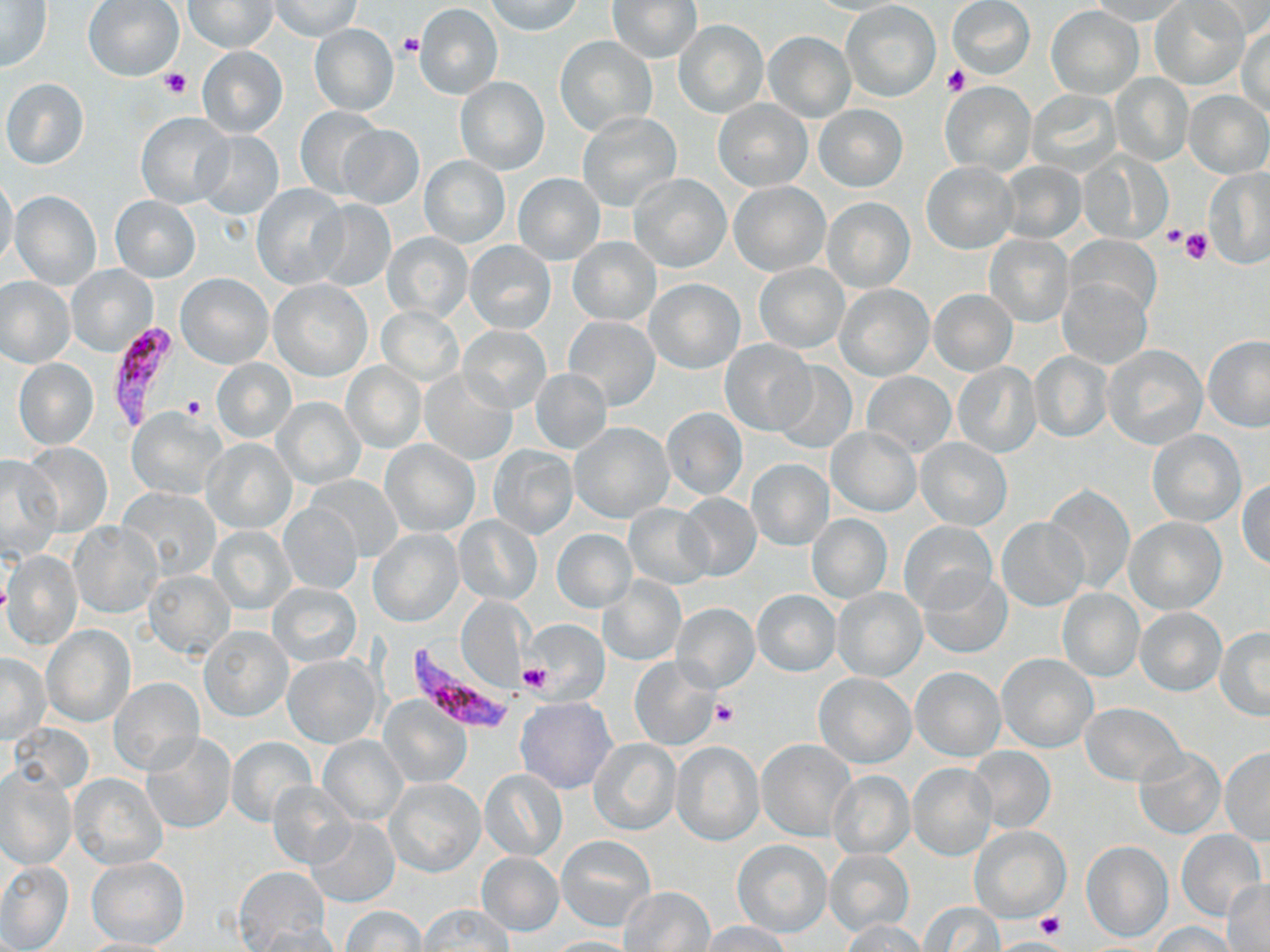

Summary:
  - Coordinate format: approximate bounding boxes as (x1,y1)-(x2,y2) corner pairs in pixels
  - Plasmodium falciparum-infected red blood cell locations: (104,322)-(182,434), (407,650)-(520,737)
  - Uninfected red blood cell locations: (83,0)-(184,82), (186,0)-(276,53), (268,0)-(362,41), (607,0)-(703,63), (948,0)-(1035,79), (1087,0)-(1190,24), (1149,0)-(1251,91), (1195,0)-(1270,40), (1,1)-(53,72), (485,1)-(584,37), (842,1)-(941,102), (415,3)-(504,98), (1046,4)-(1144,98), (674,20)-(767,118), (1238,22)-(1270,118), (309,23)-(398,116), (764,31)-(855,121), (555,35)-(657,135), (197,47)-(287,138), (1111,73)-(1192,164), (454,77)-(550,175), (1,78)-(89,169), (940,81)-(1036,175), (1026,89)-(1121,176), (1184,89)-(1269,178), (714,99)-(812,191), (814,104)-(907,191), (293,105)-(384,200), (576,112)-(681,212), (136,113)-(234,209), (337,125)-(425,209), (196,131)-(284,220), (1081,152)-(1171,245), (420,155)-(510,248), (921,162)-(1017,253), (997,162)-(1086,243), (1204,169)-(1270,268), (513,173)-(604,265), (630,173)-(731,272), (0,176)-(19,271), (729,181)-(831,277), (252,184)-(348,290), (10,191)-(102,291), (110,196)-(200,282), (823,196)-(914,291), (310,199)-(395,291), (383,231)-(474,324), (984,235)-(1073,326), (1065,235)-(1161,318), (568,238)-(660,326), (465,241)-(556,335), (755,262)-(848,353), (68,264)-(159,357), (177,273)-(273,368), (1,277)-(75,367), (8,278)-(84,451), (645,278)-(745,373), (1059,278)-(1152,368), (269,279)-(373,381), (834,284)-(934,380), (928,289)-(1018,376), (375,307)-(464,387), (562,316)-(661,412), (458,325)-(551,413), (1201,334)-(1270,433), (720,339)-(817,435), (1103,344)-(1207,449), (1029,352)-(1113,443), (13,358)-(98,449), (211,358)-(296,443), (341,361)-(425,452), (770,361)-(857,455), (952,363)-(1040,457), (420,369)-(516,465), (529,369)-(611,453), (863,372)-(955,457), (273,397)-(366,488), (660,406)-(748,501), (128,408)-(228,500), (569,422)-(674,523), (827,427)-(921,517), (1148,430)-(1246,527), (915,436)-(1012,531), (201,438)-(296,533), (381,439)-(479,537), (22,441)-(111,538), (488,446)-(578,539), (0,456)-(62,558), (746,459)-(833,550), (302,474)-(405,562), (1238,477)-(1270,570), (1044,483)-(1135,594), (120,488)-(221,578), (675,492)-(762,581), (277,502)-(362,595), (625,503)-(715,590), (807,514)-(892,603), (454,516)-(541,604), (995,517)-(1089,611), (1123,517)-(1226,615), (898,520)-(997,614), (70,522)-(161,618), (208,525)-(297,614), (368,528)-(463,627), (550,529)-(637,612), (4,551)-(82,648), (919,568)-(1011,659), (145,570)-(235,659), (598,575)-(685,666), (269,582)-(361,667), (832,588)-(928,681), (752,589)-(841,675), (1057,589)-(1144,681), (456,596)-(529,692), (672,603)-(759,692), (1134,608)-(1227,695), (526,621)-(610,705), (43,626)-(134,726), (200,626)-(292,721), (1215,627)-(1270,719), (996,652)-(1098,753), (1,654)-(49,743), (282,654)-(382,747), (629,656)-(720,751), (911,667)-(1005,760), (814,672)-(915,767), (107,677)-(203,776), (381,695)-(470,789), (516,697)-(617,794), (1079,702)-(1184,786), (141,733)-(236,835), (319,735)-(407,824), (227,736)-(316,825), (589,738)-(682,835), (756,739)-(855,841), (671,740)-(765,847), (967,746)-(1056,833), (1132,747)-(1225,839), (1219,748)-(1270,843), (907,763)-(997,860), (0,764)-(77,867), (481,768)-(568,861), (828,770)-(915,858), (70,773)-(167,869), (386,779)-(485,878), (266,780)-(357,868), (306,817)-(399,907), (970,827)-(1070,924), (1177,830)-(1265,919), (556,835)-(656,931), (732,840)-(832,937), (1082,840)-(1172,941), (825,849)-(913,937), (477,852)-(563,936), (85,855)-(188,948), (1,861)-(73,951), (234,865)-(330,948), (1222,883)-(1270,951), (621,886)-(716,951), (919,901)-(1004,950), (339,905)-(427,951), (418,905)-(512,951), (842,921)-(927,952), (702,922)-(790,952), (1151,922)-(1235,952), (251,924)-(344,951), (75,937)-(184,952), (544,937)-(638,952)
  - Platelet locations: (397,32)-(423,58), (943,64)-(969,96), (159,67)-(193,98), (1158,223)-(1189,252), (1181,228)-(1214,265), (181,395)-(206,421), (520,662)-(553,693), (713,701)-(740,727), (1036,909)-(1066,939), (995,939)-(1064,951)
  - Slide-level diagnosis: Plasmodium falciparum
  - Magnification: 1000x
  - Image size: 1270×952 pixels
  - Modality: light microscopy
  - Stain: May-Grünwald-Giemsa
  - Preparation: thin blood smear
  - Field of view: one of a larger specimen